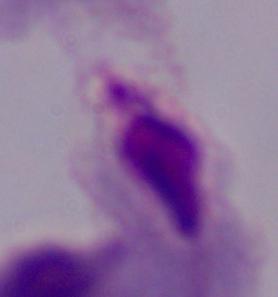
1000x magnification. A trichomonad is shown. Micrograph.